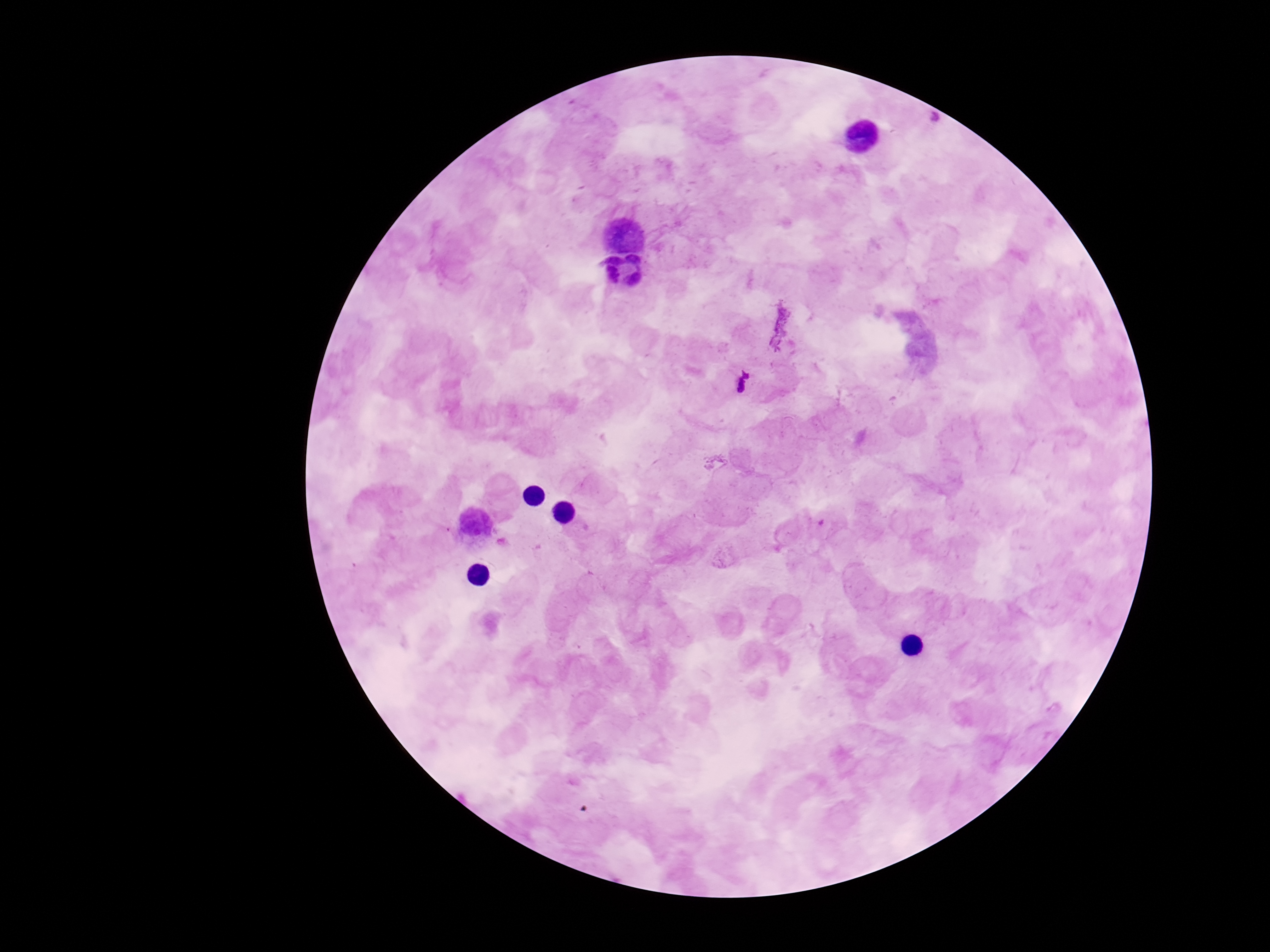
field_of_view: single
capture: smartphone camera through the microscope eyepiece
image_size: 1270×952 pixels
stain: Giemsa
plasmodium_parasite_locations: 'approximate centers as [x, y] in pixels: [935, 118], [746, 374]'
patient_malaria_status: infected
preparation: thick blood film
magnification: 100x